Locate and identify every blood parasite.
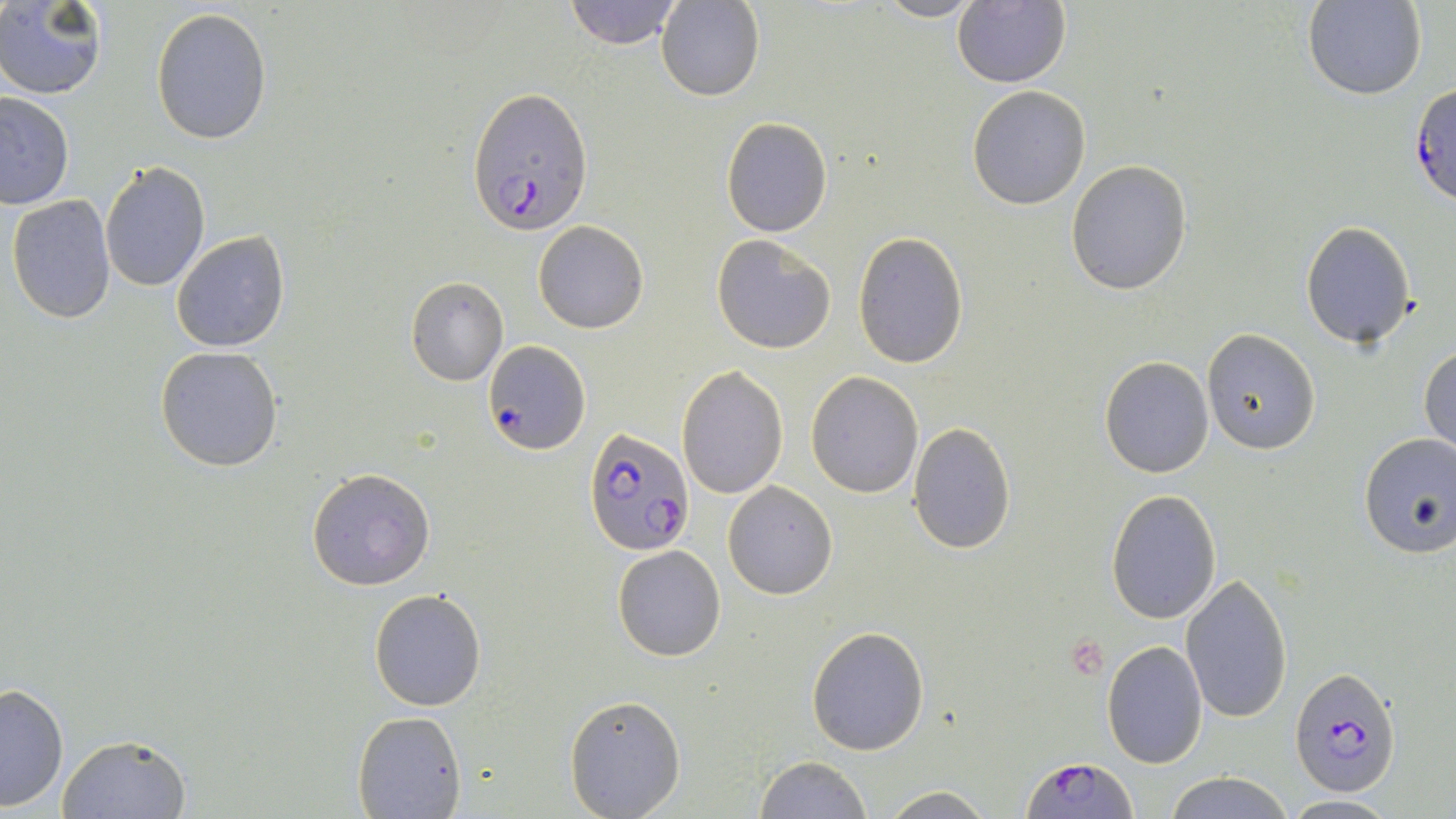

Approximate bounding boxes as [x1, y1, x2, y2] in pixels.
Plasmodium falciparum-infected red blood cells: [1409, 81, 1456, 209], [467, 89, 591, 234], [484, 341, 589, 454], [587, 427, 693, 553], [1290, 668, 1402, 796], [1021, 756, 1140, 818].
No Plasmodium ovale, Plasmodium malariae, Plasmodium vivax, Babesia divergens, or Trypanosoma brucei observed.

Uninfected red blood cell locations: [562, 0, 685, 49], [872, 0, 985, 22], [953, 0, 1070, 87], [0, 1, 107, 98], [657, 1, 765, 101], [1304, 1, 1426, 101], [151, 6, 272, 145], [967, 86, 1090, 209], [0, 91, 74, 208], [719, 117, 833, 237], [1065, 161, 1192, 296], [99, 162, 210, 290], [6, 194, 116, 323], [533, 221, 649, 334], [1299, 221, 1416, 348], [171, 232, 290, 352], [852, 232, 969, 370], [711, 234, 838, 355], [406, 277, 509, 386], [1201, 329, 1320, 455], [1419, 343, 1456, 454], [154, 345, 283, 472], [1099, 356, 1214, 477], [677, 363, 790, 501], [806, 371, 923, 498], [908, 421, 1016, 554], [1358, 432, 1456, 560], [307, 467, 436, 591], [723, 482, 836, 599], [1105, 491, 1222, 624], [611, 544, 726, 662], [1180, 572, 1295, 724], [369, 588, 488, 711], [807, 625, 930, 756], [1101, 640, 1209, 769], [0, 683, 69, 813], [565, 694, 685, 818], [352, 709, 465, 817], [58, 732, 191, 818], [754, 756, 872, 818], [1163, 772, 1295, 819], [880, 787, 996, 819], [1281, 794, 1400, 816]. Slide-level diagnosis: Plasmodium falciparum. Optical microscopy. Captured at 1000x magnification. One field of a larger specimen. May-Grünwald-Giemsa-stained preparation. Thin blood film. Image is 1456×819 pixels.